Report the malaria status of this cell.
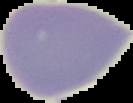
Uninfected.

Summary:
  - Preparation: thin blood smear
  - Image size: 133×103 pixels
  - Image type: segmented cell region on a black background